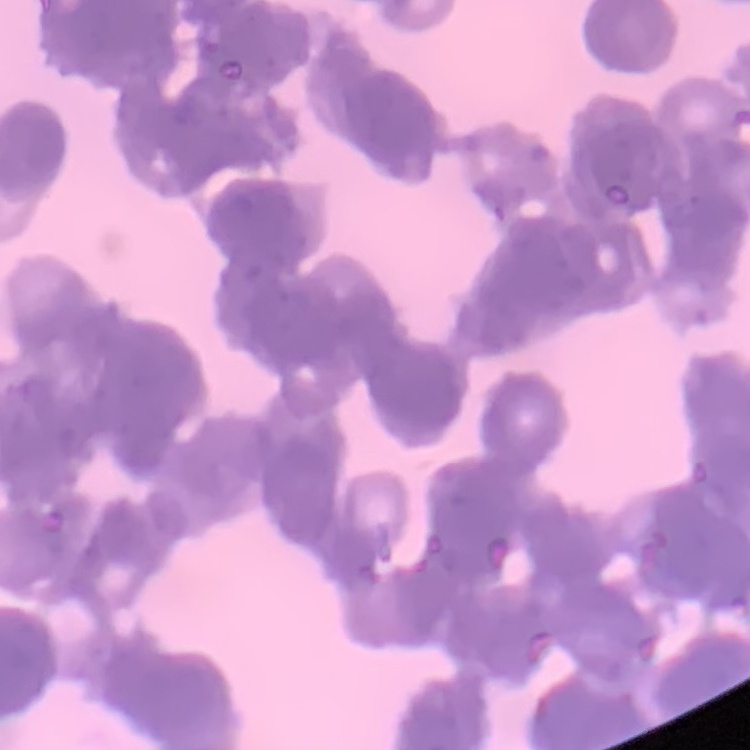

erythrocyte morphology = rouleaux formation
preparation = thin blood film
stain = Field's or Giemsa
image type = one tile cut from a larger photomicrograph